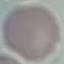
malaria status = uninfected
capture = smartphone camera at the microscope eyepiece
stain = Giemsa
preparation = thin blood smear
image type = cell patch, automatically extracted from a larger field of view and resized to 64 × 64 pixels